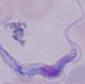

Summary:
  - Identification: trypanosome
  - Magnification: 1000x
  - Modality: photomicrograph